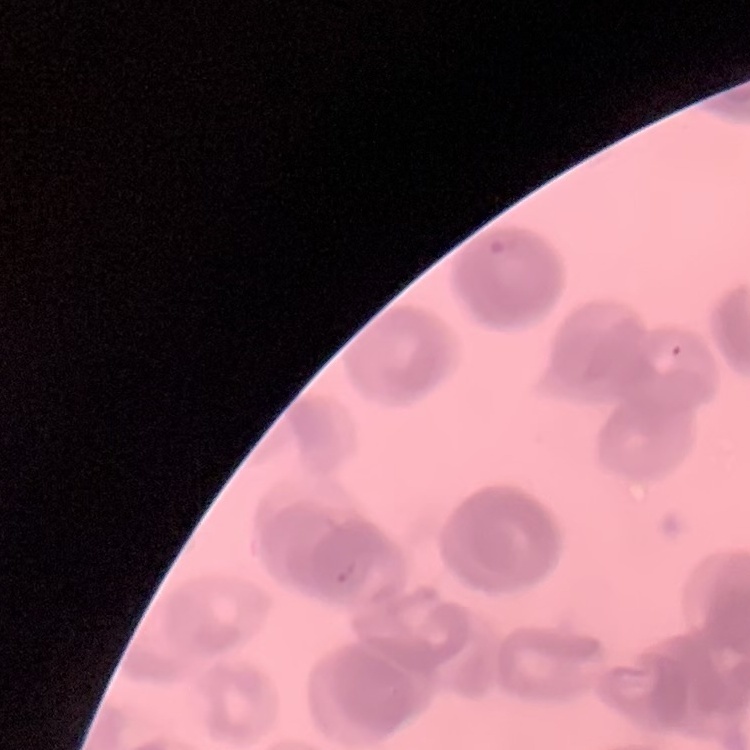
erythrocyte_morphology: rouleaux formation
stain: Field's or Giemsa
preparation: thin blood smear
image_type: square crop of a larger photomicrograph